Report the malaria status of this cell.
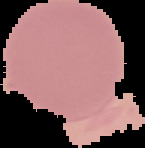

It is uninfected.

Segmented cell region on a black background. Image is 145×148 pixels. From a thin blood film.